Outline each blood parasite and name the species.
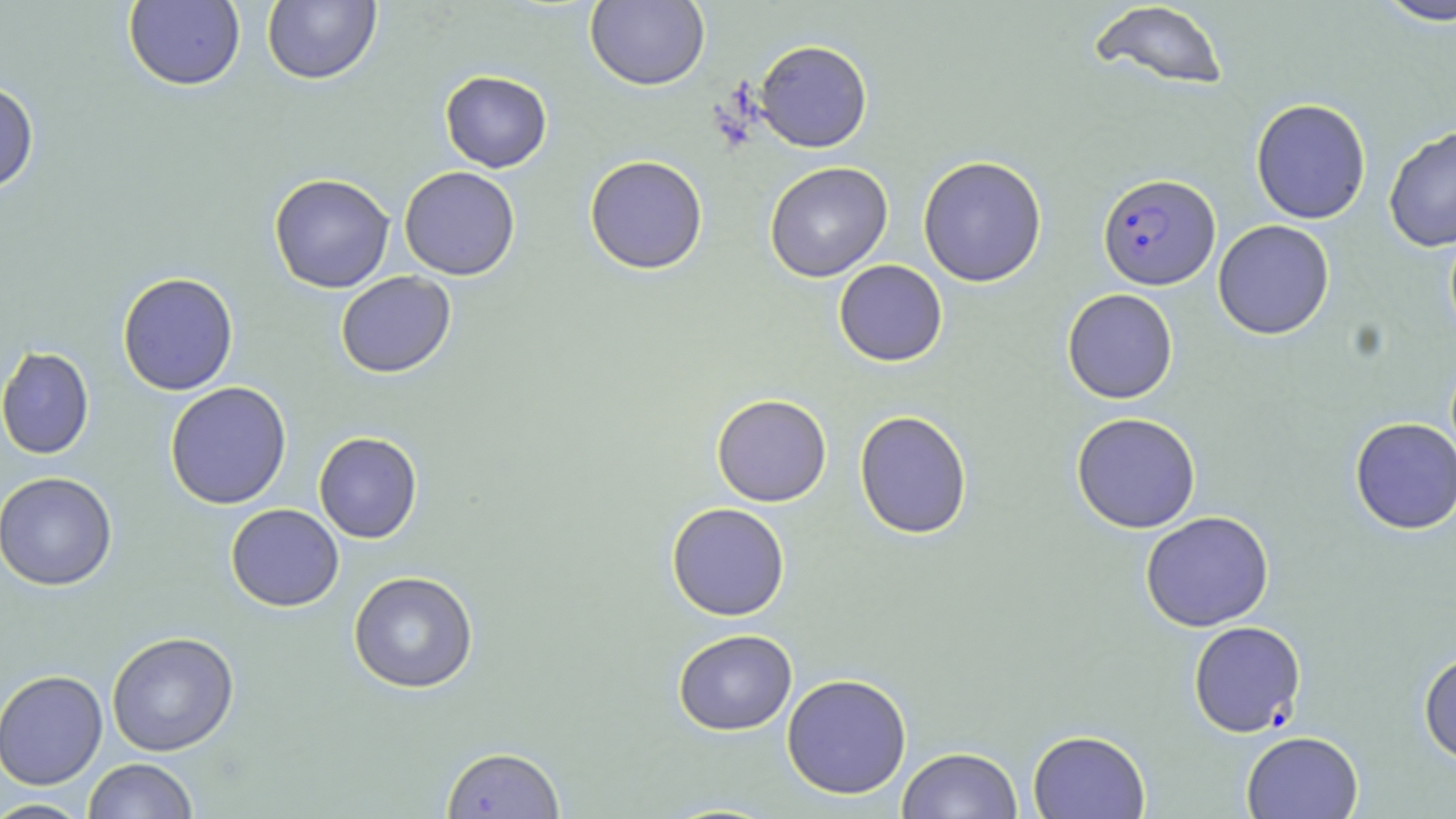

Approximate bounding boxes as (x1,y1)-(x2,y2) corner pairs in pixels.
Plasmodium falciparum-infected red blood cells: (1098,173)-(1220,290).
No Plasmodium ovale, Plasmodium malariae, Plasmodium vivax, Babesia divergens, or Trypanosoma brucei observed.

Uninfected red blood cell locations: (262,0)-(381,85), (1372,0)-(1456,27), (123,1)-(246,91), (585,1)-(709,91), (1086,2)-(1230,91), (754,39)-(872,153), (440,70)-(552,172), (0,79)-(39,195), (1250,98)-(1371,224), (1384,125)-(1456,252), (584,155)-(708,274), (917,155)-(1047,287), (764,161)-(893,282), (399,166)-(521,280), (269,173)-(396,293), (1213,220)-(1334,340), (833,260)-(948,366), (335,271)-(456,378), (117,272)-(239,396), (1062,288)-(1178,404), (0,346)-(94,459), (165,381)-(292,509), (711,393)-(831,507), (854,410)-(973,539), (1071,412)-(1201,533), (1349,417)-(1456,535), (313,431)-(423,543), (0,471)-(118,590), (666,502)-(790,621), (226,503)-(344,611), (1140,511)-(1274,632), (348,571)-(479,693), (1188,620)-(1306,737), (672,629)-(798,735), (106,631)-(239,756), (1418,650)-(1456,763), (0,670)-(108,790), (781,673)-(912,799), (1027,729)-(1150,819), (1241,731)-(1363,818), (441,746)-(565,818), (897,746)-(1023,819), (83,758)-(199,819), (0,798)-(93,818). Slide-level diagnosis: Plasmodium falciparum. Image is 1456×819 pixels. May-Grünwald-Giemsa-stained preparation. Single field of view. 1000x magnification. Thin blood film. Optical microscopy.